Classify this cell by malaria status.
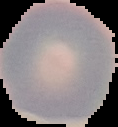

Uninfected.

Image is 118×127 pixels. From a thin blood film. Segmented cell region on a black background.